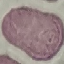

malaria_status: uninfected
stain: Giemsa
capture: smartphone through the microscope eyepiece
preparation: thin blood smear
image_type: cell patch, automatically extracted from a larger field of view and resized to 64 × 64 pixels